Assess the morphology of the erythrocytes.
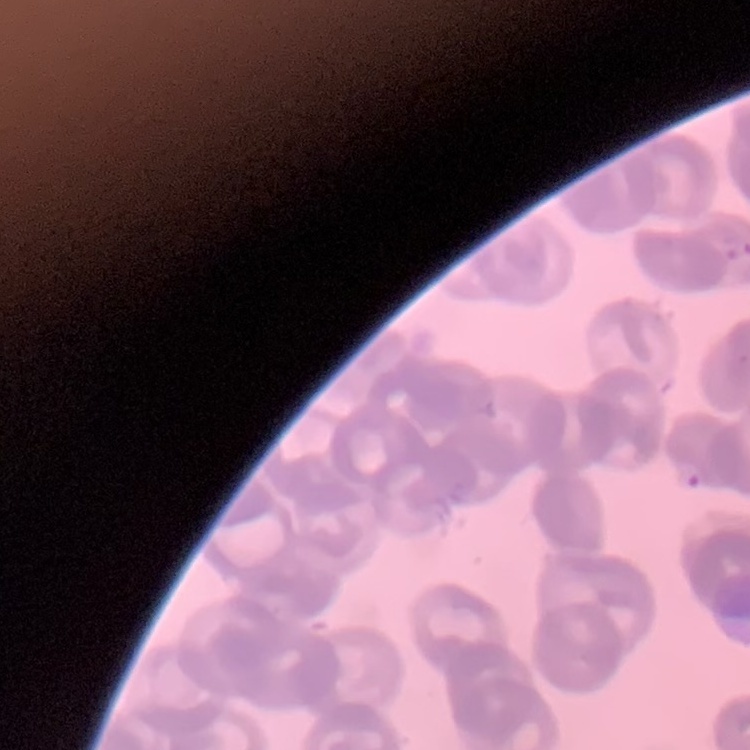
Rouleaux formation.

Summary:
  - Preparation: thin blood smear
  - Image type: one tile cut from a larger photomicrograph
  - Stain: Field's or Giemsa